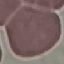 Malaria status: uninfected. Photographed with a smartphone camera at the microscope eyepiece. Thin blood smear. Cell patch, automatically extracted from a larger field of view and resized to 64 × 64 pixels. Giemsa-stained preparation.